Classify this cell by malaria status.
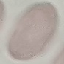

Uninfected.

{
  "stain": "Giemsa",
  "capture": "smartphone camera at the microscope eyepiece",
  "preparation": "thin smear",
  "image_type": "cell patch, automatically extracted from a larger field of view and resized to 64 × 64 pixels"
}